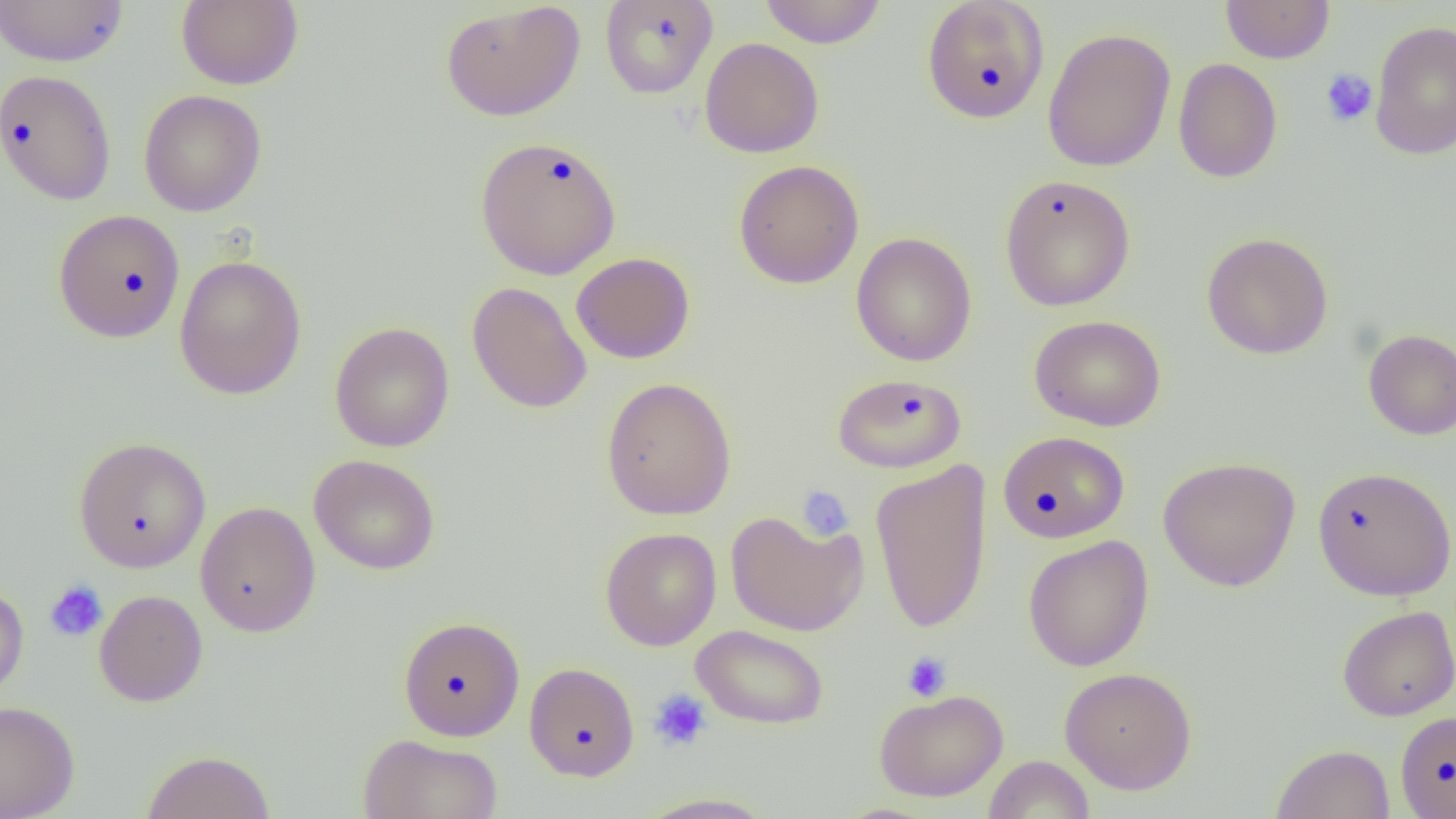

Summary:
  - Coordinate format: approximate bounding boxes as named x1/y1/x2/y2 corners in pixels
  - Platelet locations: (x1=1320, y1=68, x2=1378, y2=127), (x1=796, y1=485, x2=854, y2=541), (x1=44, y1=580, x2=109, y2=642), (x1=902, y1=651, x2=952, y2=701), (x1=648, y1=688, x2=713, y2=751)
  - Uninfected red blood cell locations: (x1=0, y1=0, x2=129, y2=67), (x1=176, y1=0, x2=304, y2=90), (x1=599, y1=0, x2=718, y2=99), (x1=758, y1=0, x2=888, y2=48), (x1=921, y1=0, x2=1050, y2=124), (x1=440, y1=1, x2=585, y2=122), (x1=1220, y1=1, x2=1335, y2=64), (x1=1369, y1=20, x2=1456, y2=160), (x1=1042, y1=27, x2=1176, y2=172), (x1=699, y1=38, x2=825, y2=158), (x1=1172, y1=57, x2=1283, y2=183), (x1=0, y1=69, x2=117, y2=205), (x1=138, y1=89, x2=267, y2=217), (x1=474, y1=135, x2=622, y2=280), (x1=733, y1=159, x2=864, y2=289), (x1=999, y1=174, x2=1136, y2=312), (x1=53, y1=208, x2=186, y2=343), (x1=1201, y1=231, x2=1334, y2=360), (x1=851, y1=232, x2=977, y2=367), (x1=571, y1=252, x2=695, y2=364), (x1=174, y1=254, x2=307, y2=400), (x1=467, y1=282, x2=592, y2=414), (x1=1029, y1=315, x2=1166, y2=432), (x1=330, y1=322, x2=454, y2=452), (x1=1363, y1=329, x2=1456, y2=440), (x1=832, y1=372, x2=964, y2=474), (x1=601, y1=376, x2=737, y2=520), (x1=998, y1=431, x2=1129, y2=543), (x1=73, y1=436, x2=211, y2=573), (x1=309, y1=454, x2=440, y2=575), (x1=1158, y1=456, x2=1300, y2=591), (x1=869, y1=459, x2=992, y2=635), (x1=1311, y1=465, x2=1455, y2=600), (x1=195, y1=501, x2=320, y2=637), (x1=724, y1=509, x2=868, y2=636), (x1=599, y1=527, x2=722, y2=650), (x1=1023, y1=535, x2=1154, y2=672), (x1=0, y1=585, x2=29, y2=703), (x1=94, y1=589, x2=208, y2=707), (x1=1336, y1=605, x2=1456, y2=721), (x1=398, y1=616, x2=525, y2=741), (x1=691, y1=624, x2=830, y2=730), (x1=524, y1=662, x2=639, y2=781), (x1=1059, y1=666, x2=1197, y2=794), (x1=873, y1=688, x2=1008, y2=802), (x1=0, y1=701, x2=79, y2=818), (x1=1395, y1=710, x2=1456, y2=818), (x1=358, y1=733, x2=504, y2=819), (x1=1270, y1=744, x2=1395, y2=819), (x1=141, y1=750, x2=276, y2=819), (x1=984, y1=754, x2=1095, y2=818), (x1=635, y1=792, x2=778, y2=818)
  - Slide-level diagnosis: no evidence of blood parasites
  - Preparation: thin blood smear
  - Modality: optical microscopy
  - Field of view: single
  - Image size: 1456×819 pixels
  - Magnification: 1000x